Outline each uninfected red blood cell.
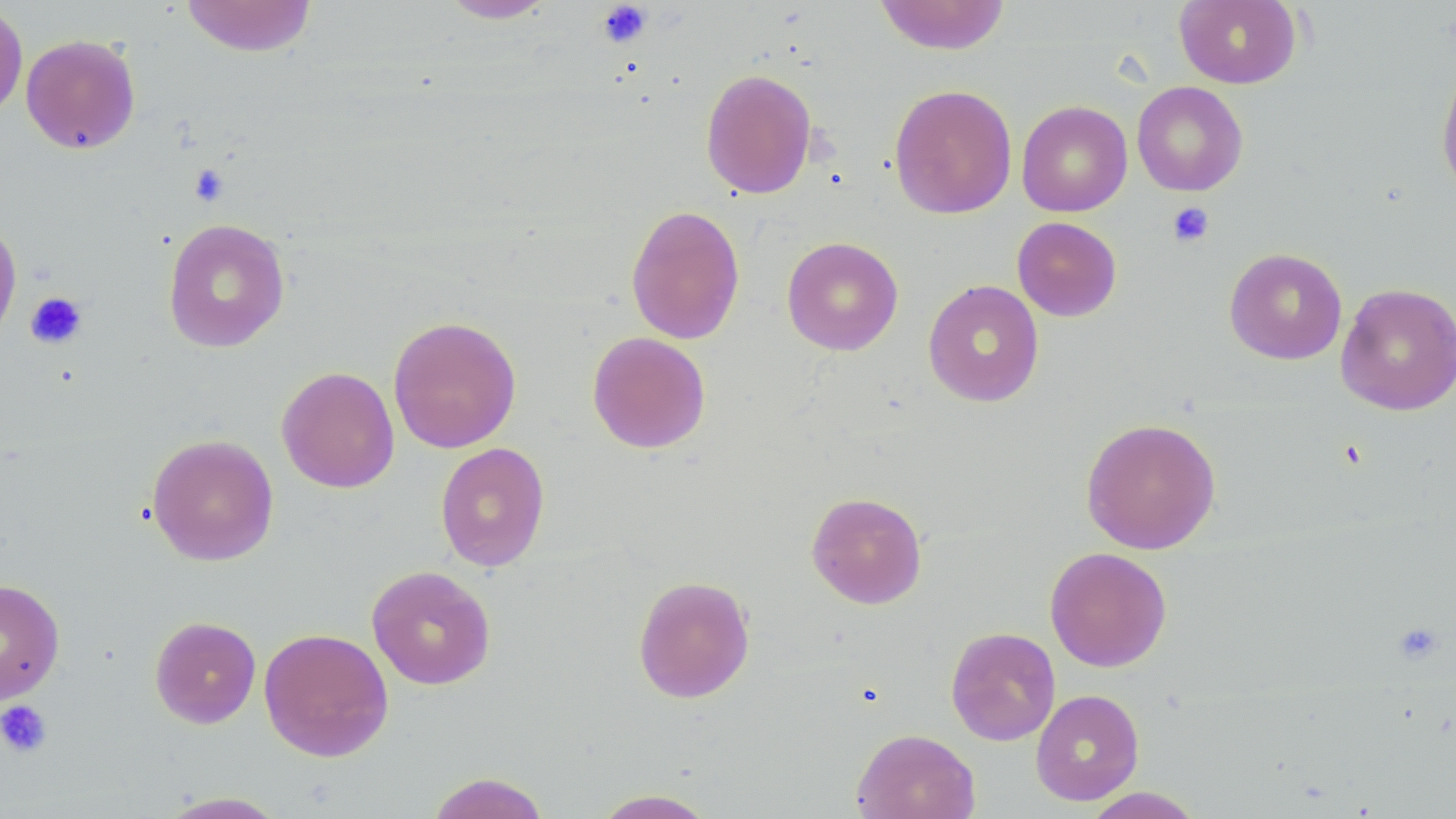

Approximate bounding boxes as [x1, y1, x2, y2] in pixels.
Uninfected red blood cells: [181, 0, 317, 58], [437, 0, 557, 24], [874, 0, 1012, 55], [1174, 0, 1302, 89], [0, 4, 29, 122], [20, 34, 141, 155], [1435, 62, 1456, 203], [700, 68, 817, 199], [1132, 81, 1248, 196], [889, 84, 1017, 219], [1016, 100, 1132, 217], [625, 204, 745, 345], [0, 216, 21, 348], [1011, 216, 1122, 322], [162, 218, 290, 353], [781, 236, 904, 356], [1224, 247, 1347, 365], [923, 279, 1044, 407], [1335, 282, 1456, 416], [387, 315, 522, 454], [587, 331, 711, 454], [277, 366, 399, 493], [1080, 418, 1221, 554], [146, 433, 279, 566], [435, 442, 550, 571], [806, 491, 927, 609], [1045, 546, 1172, 672], [367, 565, 496, 690], [632, 575, 755, 703], [0, 578, 65, 705], [149, 615, 261, 728], [945, 626, 1060, 746], [258, 627, 394, 762], [1030, 688, 1144, 806], [851, 728, 980, 819], [425, 772, 552, 819], [1082, 787, 1204, 818], [591, 788, 719, 818], [157, 791, 290, 818].

slide-level diagnosis = no evidence of blood parasites
field of view = one of a larger specimen
modality = light microscopy
preparation = thin blood smear
image size = 1456×819 pixels
magnification = 1000x
stain = May-Grünwald-Giemsa
platelet locations = approximate bounding boxes as [x1, y1, x2, y2] in pixels: [596, 1, 653, 49], [188, 164, 229, 207], [1167, 202, 1215, 248], [25, 291, 88, 349], [1392, 622, 1445, 665], [0, 699, 52, 758]